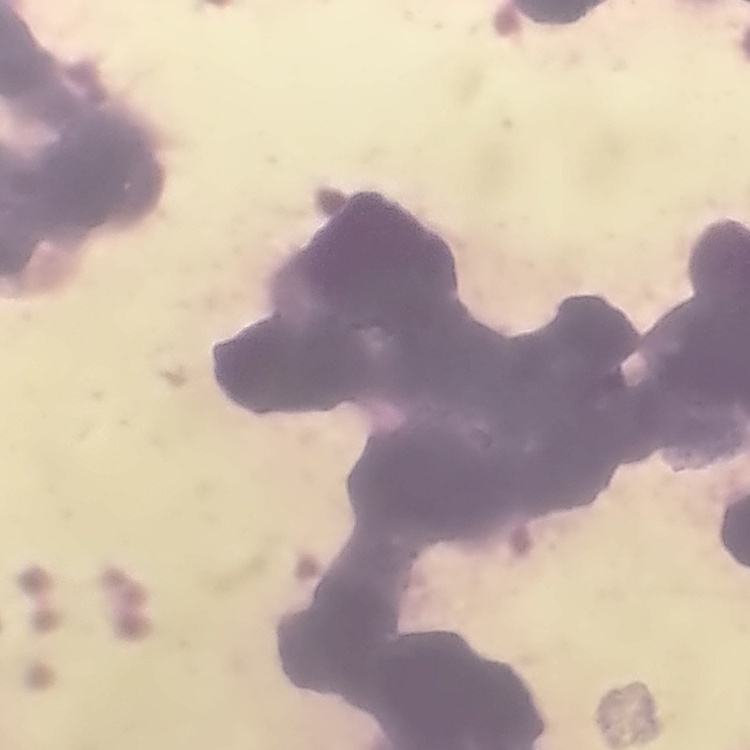
{
  "erythrocyte_morphology": "rouleaux formation",
  "image_type": "square crop of a larger photomicrograph",
  "stain": "Field's or Giemsa",
  "preparation": "thin peripheral smear"
}